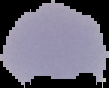
image size = 109×88 pixels
preparation = thin blood film
malaria status = uninfected
image type = segmented cell region on a black background